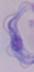
Summary:
  - Modality: micrograph
  - Identification: trypanosome
  - Magnification: 1000x